Classify this cell by malaria status.
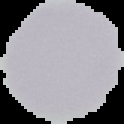
It is uninfected.

image_type: segmented cell region on a black background
preparation: thin blood smear
image_size: 124×124 pixels